Outline each Plasmodium ovale-infected red blood cell.
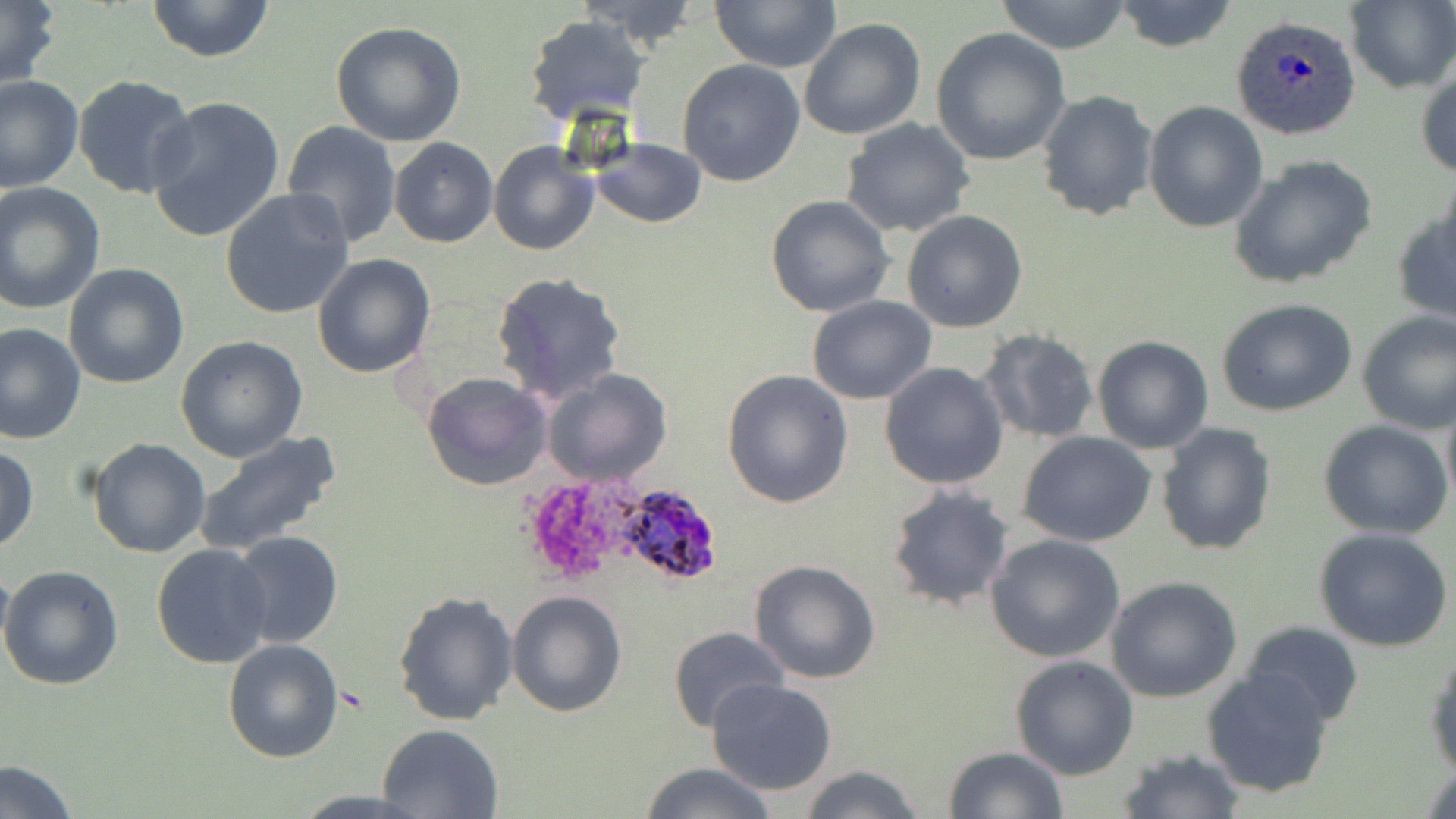
Approximate bounding boxes as (x1, y1, x2, y2) in pixels.
Plasmodium ovale-infected red blood cells: (1232, 14, 1363, 140), (611, 482, 722, 587).

Summary:
  - Platelet locations: (518, 483, 616, 581)
  - Uninfected red blood cell locations: (0, 0, 59, 90), (146, 0, 275, 64), (567, 0, 704, 46), (711, 0, 841, 73), (994, 0, 1134, 54), (1112, 0, 1239, 53), (1344, 0, 1456, 94), (523, 14, 649, 127), (799, 17, 926, 140), (330, 20, 467, 147), (931, 28, 1070, 164), (677, 59, 805, 187), (1416, 64, 1456, 183), (0, 73, 84, 192), (73, 75, 198, 201), (1037, 89, 1160, 222), (145, 94, 287, 243), (1143, 100, 1268, 232), (840, 118, 975, 238), (279, 120, 402, 249), (389, 138, 498, 249), (591, 139, 706, 229), (488, 140, 599, 256), (1228, 154, 1377, 289), (0, 182, 105, 314), (220, 188, 356, 321), (764, 194, 896, 317), (1391, 200, 1456, 328), (902, 210, 1029, 332), (312, 253, 436, 377), (63, 263, 190, 389), (492, 272, 626, 402), (806, 295, 936, 404), (1217, 299, 1359, 418), (1356, 311, 1456, 434), (0, 322, 86, 444), (978, 327, 1101, 445), (177, 335, 307, 462), (1092, 336, 1215, 454), (880, 362, 1008, 489), (543, 368, 673, 486), (721, 369, 855, 507), (422, 372, 552, 492), (1440, 390, 1456, 513), (1319, 418, 1453, 539), (1155, 422, 1277, 557), (194, 431, 343, 555), (1017, 431, 1157, 547), (88, 437, 211, 558), (0, 446, 39, 552), (885, 483, 1016, 610), (1313, 526, 1452, 652), (230, 530, 344, 650), (984, 532, 1127, 664), (151, 543, 274, 667), (0, 558, 13, 670), (748, 559, 881, 684), (0, 564, 124, 690), (1105, 575, 1243, 702), (393, 589, 520, 725), (507, 589, 629, 718), (1242, 620, 1363, 726), (667, 625, 789, 732), (222, 637, 343, 763), (1425, 643, 1456, 777), (1010, 654, 1139, 781), (1200, 666, 1336, 799), (705, 676, 838, 795), (376, 722, 506, 818), (943, 745, 1068, 819), (1116, 747, 1245, 819), (0, 757, 80, 819), (639, 763, 778, 819), (798, 763, 927, 819)
  - Slide-level diagnosis: Plasmodium ovale
  - Magnification: 1000x
  - Field of view: one of a larger specimen
  - Modality: optical microscopy
  - Preparation: thin blood film
  - Image size: 1456×819 pixels
  - Stain: May-Grünwald-Giemsa